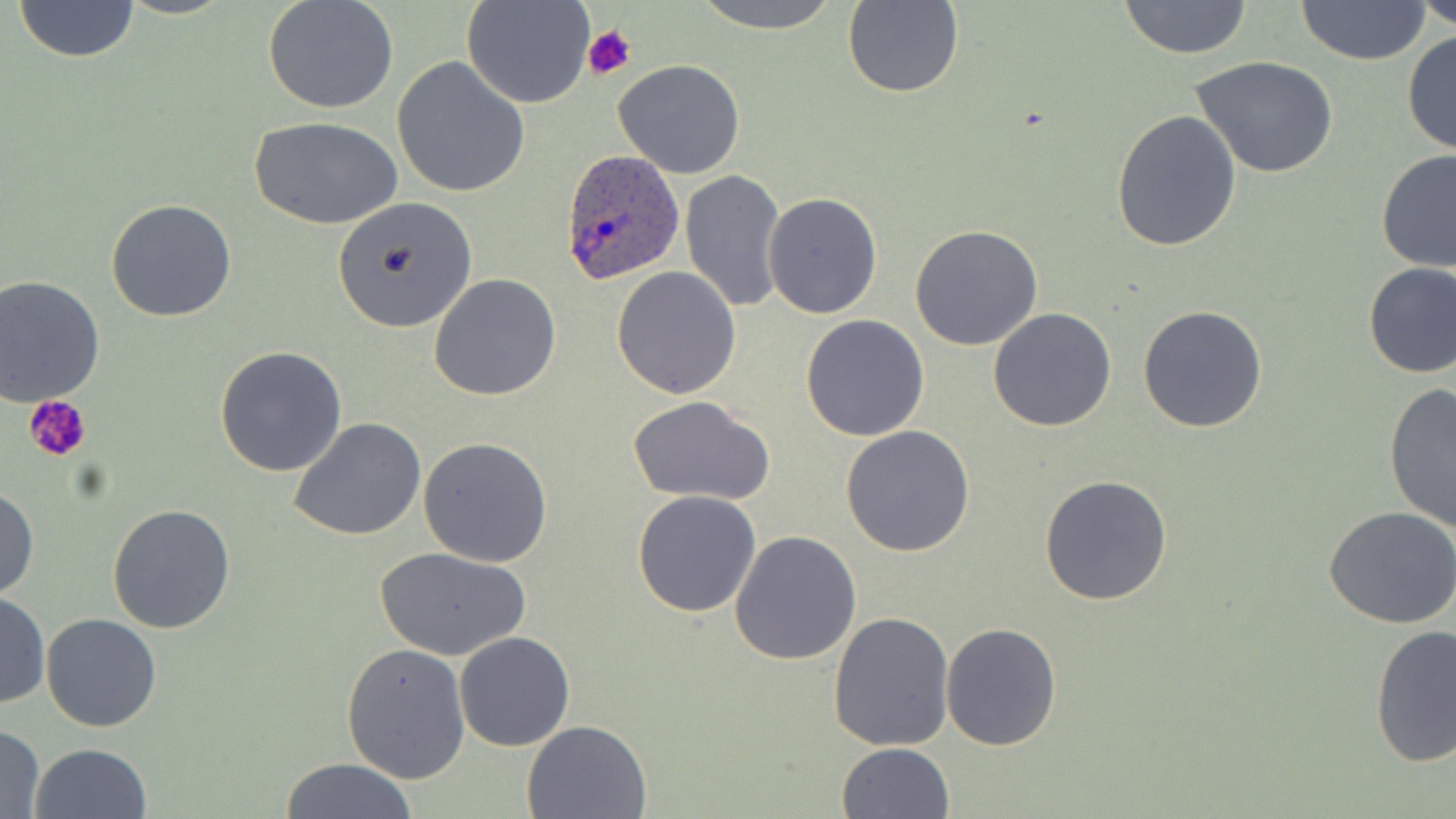

Approximate bounding boxes as named x1/y1/x2/y2 corners in pixels. Uninfected red blood cell locations: (x1=263, y1=0, x2=398, y2=115), (x1=463, y1=0, x2=596, y2=108), (x1=689, y1=0, x2=845, y2=33), (x1=1117, y1=0, x2=1255, y2=58), (x1=1296, y1=0, x2=1430, y2=65), (x1=1418, y1=0, x2=1456, y2=31), (x1=12, y1=1, x2=143, y2=62), (x1=843, y1=1, x2=964, y2=99), (x1=1403, y1=31, x2=1456, y2=160), (x1=1189, y1=55, x2=1339, y2=178), (x1=392, y1=57, x2=529, y2=199), (x1=613, y1=59, x2=745, y2=179), (x1=1111, y1=108, x2=1241, y2=252), (x1=249, y1=116, x2=404, y2=230), (x1=1377, y1=148, x2=1456, y2=274), (x1=681, y1=169, x2=785, y2=313), (x1=763, y1=192, x2=883, y2=319), (x1=332, y1=197, x2=478, y2=333), (x1=106, y1=198, x2=236, y2=322), (x1=910, y1=226, x2=1044, y2=350), (x1=1360, y1=261, x2=1455, y2=379), (x1=610, y1=265, x2=742, y2=398), (x1=429, y1=273, x2=561, y2=401), (x1=0, y1=276, x2=104, y2=405), (x1=1137, y1=305, x2=1269, y2=433), (x1=987, y1=307, x2=1116, y2=432), (x1=801, y1=315, x2=929, y2=441), (x1=214, y1=346, x2=347, y2=477), (x1=1383, y1=379, x2=1456, y2=531), (x1=627, y1=394, x2=775, y2=506), (x1=287, y1=416, x2=427, y2=540), (x1=840, y1=425, x2=976, y2=557), (x1=419, y1=437, x2=552, y2=567), (x1=1040, y1=475, x2=1173, y2=606), (x1=0, y1=486, x2=38, y2=600), (x1=632, y1=490, x2=762, y2=617), (x1=107, y1=503, x2=236, y2=633), (x1=1323, y1=505, x2=1456, y2=629), (x1=728, y1=529, x2=862, y2=666), (x1=374, y1=547, x2=531, y2=660), (x1=0, y1=593, x2=50, y2=708), (x1=828, y1=611, x2=955, y2=751), (x1=41, y1=613, x2=161, y2=731), (x1=941, y1=623, x2=1064, y2=752), (x1=1369, y1=625, x2=1454, y2=767), (x1=454, y1=631, x2=576, y2=751), (x1=342, y1=644, x2=471, y2=784), (x1=521, y1=718, x2=653, y2=819), (x1=0, y1=724, x2=45, y2=819), (x1=836, y1=742, x2=955, y2=819), (x1=29, y1=743, x2=152, y2=819), (x1=278, y1=757, x2=418, y2=819). Platelet locations: (x1=583, y1=24, x2=638, y2=83), (x1=26, y1=396, x2=94, y2=463). Plasmodium ovale-infected red blood cell locations: (x1=558, y1=148, x2=687, y2=288). Slide-level diagnosis: Plasmodium ovale. May-Grünwald-Giemsa-stained preparation. Image is 1456×819 pixels. Thin blood film. Single field of view. Light microscopy. Captured at 1000x magnification.